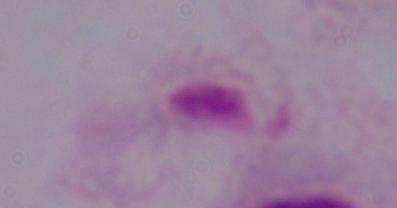
Summary:
  - Magnification: 1000x
  - Identification: trichomonad
  - Modality: photomicrograph